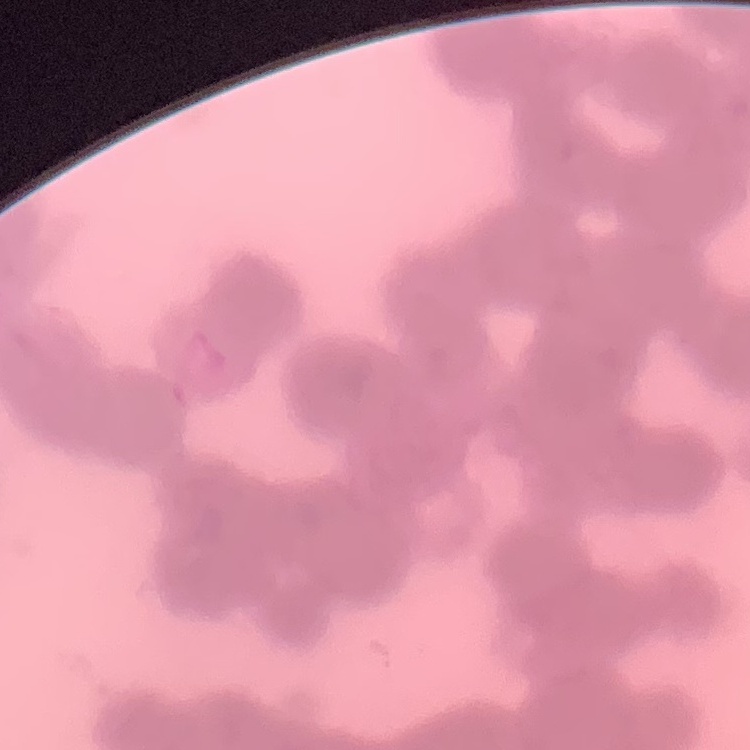
The red blood cells show rouleaux formation. Thin blood smear. Square crop of a larger photomicrograph. Field's or Giemsa stain.